Outline each Plasmodium malariae-infected red blood cell.
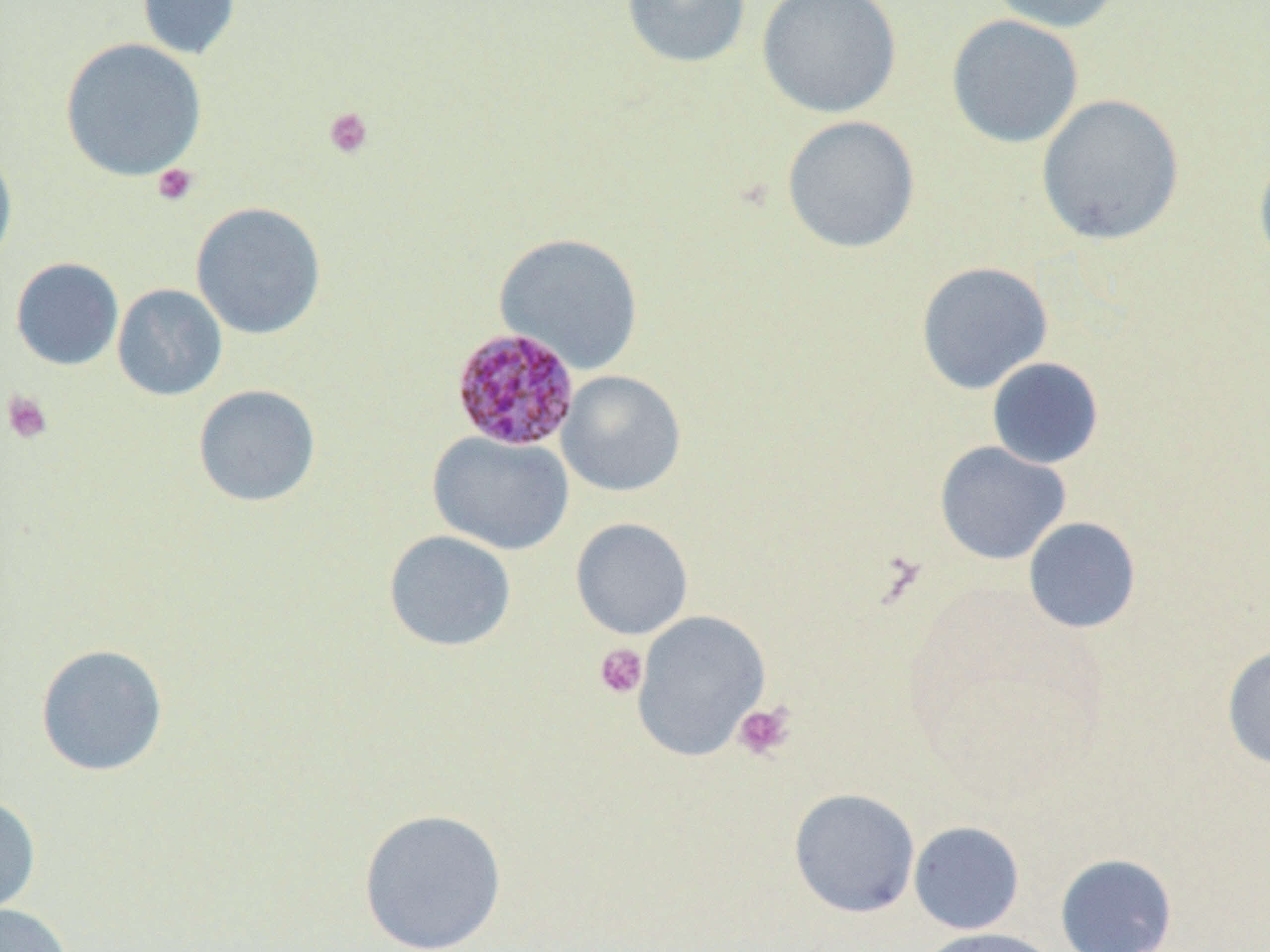

Approximate bounding boxes as (x1,y1)-(x2,y2) corner pairs in pixels.
Plasmodium malariae-infected red blood cells: (450,326)-(581,452).

{
  "slide_level_diagnosis": "Plasmodium malariae",
  "platelet_locations": "approximate bounding boxes as (x1,y1)-(x2,y2) corner pairs in pixels: (324,107)-(374,159), (151,163)-(199,206), (2,390)-(53,444), (594,643)-(649,699), (732,702)-(795,761)",
  "uninfected_red_blood_cell_locations": "approximate bounding boxes as (x1,y1)-(x2,y2) corner pairs in pixels: (137,0)-(241,61), (620,0)-(752,69), (757,0)-(902,118), (986,0)-(1125,34), (946,14)-(1084,149), (59,37)-(207,182), (1035,93)-(1185,245), (781,115)-(921,254), (1253,144)-(1270,275), (0,145)-(18,271), (191,201)-(327,339), (493,233)-(644,374), (10,257)-(124,370), (915,261)-(1053,395), (112,283)-(228,401), (987,357)-(1104,469), (556,370)-(687,496), (192,384)-(321,507), (427,431)-(574,556), (934,441)-(1071,565), (1022,516)-(1142,634), (570,518)-(693,639), (383,530)-(517,652), (632,610)-(771,761), (35,643)-(169,777), (1221,643)-(1270,771), (788,788)-(920,917), (0,793)-(42,920), (357,807)-(508,952), (908,821)-(1025,935), (1054,853)-(1178,952), (0,903)-(73,952), (917,927)-(1060,952)",
  "image_size": "1270×952 pixels",
  "field_of_view": "one of a larger specimen",
  "preparation": "thin blood smear",
  "modality": "light microscopy",
  "magnification": "1000x"
}